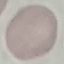

malaria status = uninfected
image type = cell patch, automatically extracted from a larger field of view and resized to 64 × 64 pixels
preparation = thin blood smear
stain = Giemsa
capture = smartphone through the microscope eyepiece